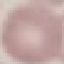
result = no malaria parasites seen
preparation = thin blood smear
stain = Giemsa
capture = smartphone through the microscope eyepiece
image type = automatically extracted cell patch, resized to 64 × 64 pixels